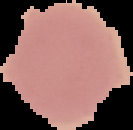

Summary:
  - Image size: 133×130 pixels
  - Image type: cell region segmented out of the field of view; surrounding area masked to black
  - Preparation: thin blood smear
  - Malaria status: uninfected